Report the malaria status of this cell.
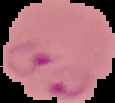
Parasitized.

image type = segmented cell region with the area outside set to black
image size = 115×103 pixels
preparation = thin blood film